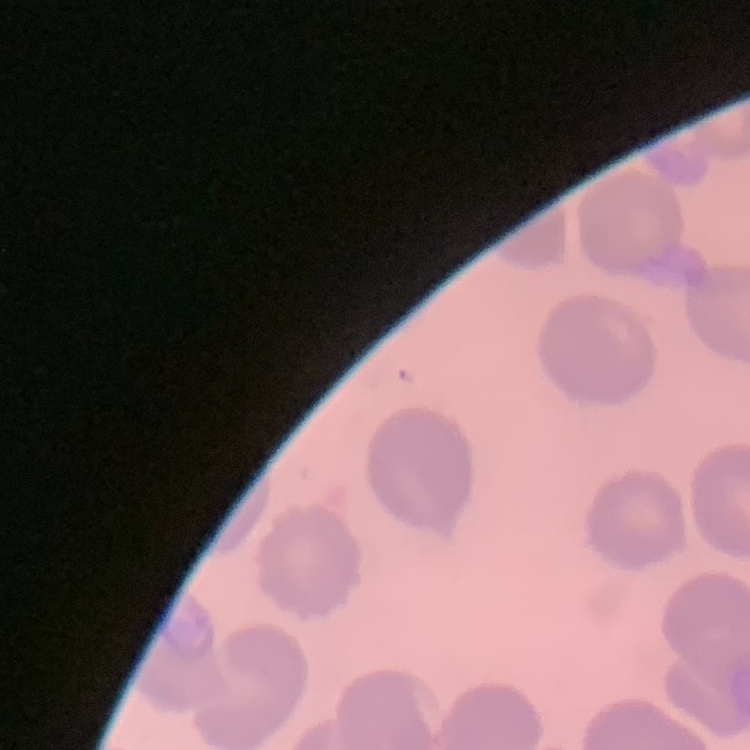

Summary:
  - Red blood cell morphology: no rouleaux formation
  - Preparation: thin blood film
  - Image type: square crop of a larger photomicrograph
  - Stain: Field's or Giemsa